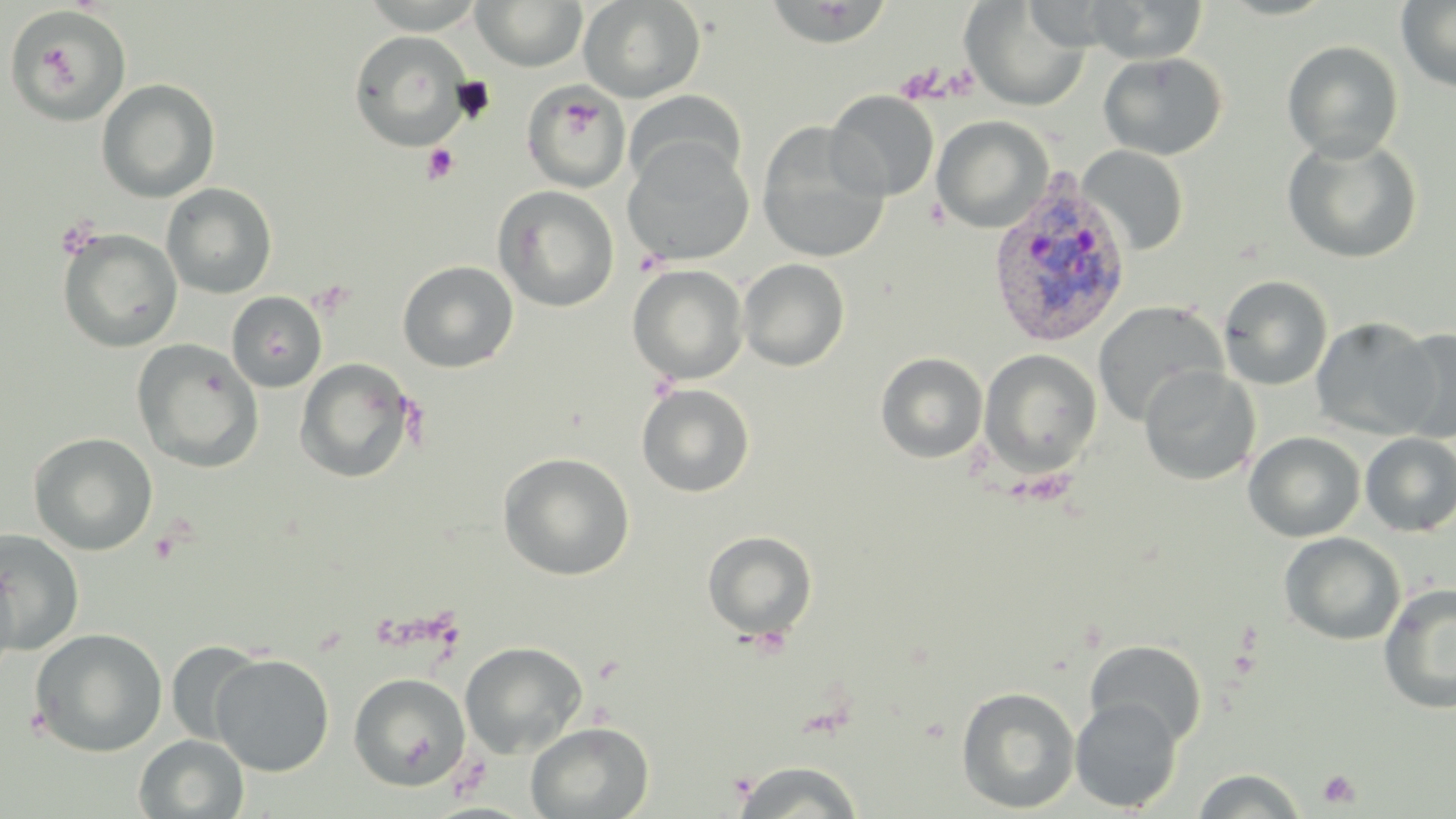
slide_level_diagnosis: Plasmodium vivax
modality: optical microscopy
field_of_view: single
stain: May-Grünwald-Giemsa
uninfected_red_blood_cell_locations: 'approximate bounding boxes as (x1,y1)-(x2,y2) corner pairs in pixels: (359,0)-(488,34), (471,0)-(588,71), (579,0)-(706,103), (1082,0)-(1209,63), (1396,0)-(1456,93), (760,1)-(894,47), (962,2)-(1090,111), (9,6)-(129,126), (348,30)-(475,151), (1281,40)-(1404,162), (1099,51)-(1227,160), (96,78)-(220,203), (521,81)-(631,192), (623,89)-(746,191), (825,90)-(939,201), (932,115)-(1053,233), (757,122)-(891,264), (1282,135)-(1423,264), (623,139)-(754,265), (1078,145)-(1189,255), (161,182)-(278,299), (493,185)-(619,312), (57,229)-(183,352), (738,258)-(850,371), (397,260)-(519,373), (628,264)-(748,384), (1218,274)-(1334,391), (226,291)-(327,392), (1092,299)-(1228,428), (1311,317)-(1439,439), (1388,326)-(1455,443), (132,339)-(264,473), (979,349)-(1102,478), (876,352)-(989,463), (295,358)-(415,483), (1139,365)-(1260,486), (636,383)-(755,497), (1243,431)-(1366,542), (28,432)-(158,555), (1360,433)-(1456,537), (497,452)-(635,581), (0,529)-(85,655), (702,530)-(818,640), (1279,532)-(1406,645), (0,560)-(20,682), (1378,582)-(1456,715), (29,627)-(168,757), (1084,639)-(1207,746), (165,640)-(267,746), (459,641)-(588,758), (210,653)-(335,776), (348,673)-(471,790), (956,686)-(1081,814), (1070,696)-(1183,813), (525,721)-(654,818), (133,734)-(249,818), (731,760)-(865,818), (1191,768)-(1308,818)'
platelet_locations: 'approximate bounding boxes as (x1,y1)-(x2,y2) corner pairs in pixels: (421,143)-(459,185), (54,216)-(101,258), (148,530)-(182,564), (1318,770)-(1361,808)'
plasmodium_vivax_infected_red_blood_cell_locations: 'approximate bounding boxes as (x1,y1)-(x2,y2) corner pairs in pixels: (987,168)-(1133,351)'
image_size: 1456×819 pixels
magnification: 1000x
preparation: thin blood smear